State which parasite is depicted.
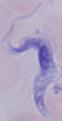

This is a trypanosome.

Summary:
  - Magnification: 1000x
  - Modality: photomicrograph